Assess this cell for malaria.
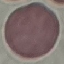

It is uninfected.

preparation = thin blood film
image type = cell patch, automatically extracted from a larger field of view and resized to 64 × 64 pixels
stain = Giemsa
capture = smartphone camera at the microscope eyepiece